Name the parasite shown.
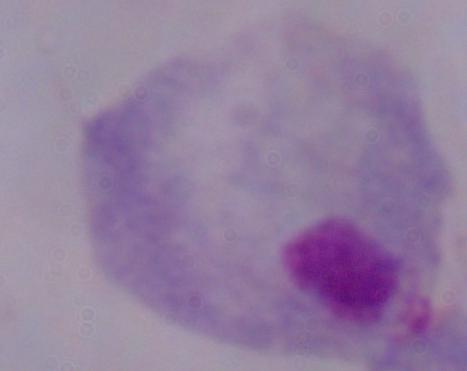
This is a trichomonad.

Captured at 1000x magnification. Micrograph.